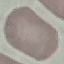
Result: no malaria parasites detected. Automatically extracted cell patch, resized to 64 × 64 pixels. Giemsa-stained preparation. Acquired by smartphone through the microscope eyepiece. Thin blood film.